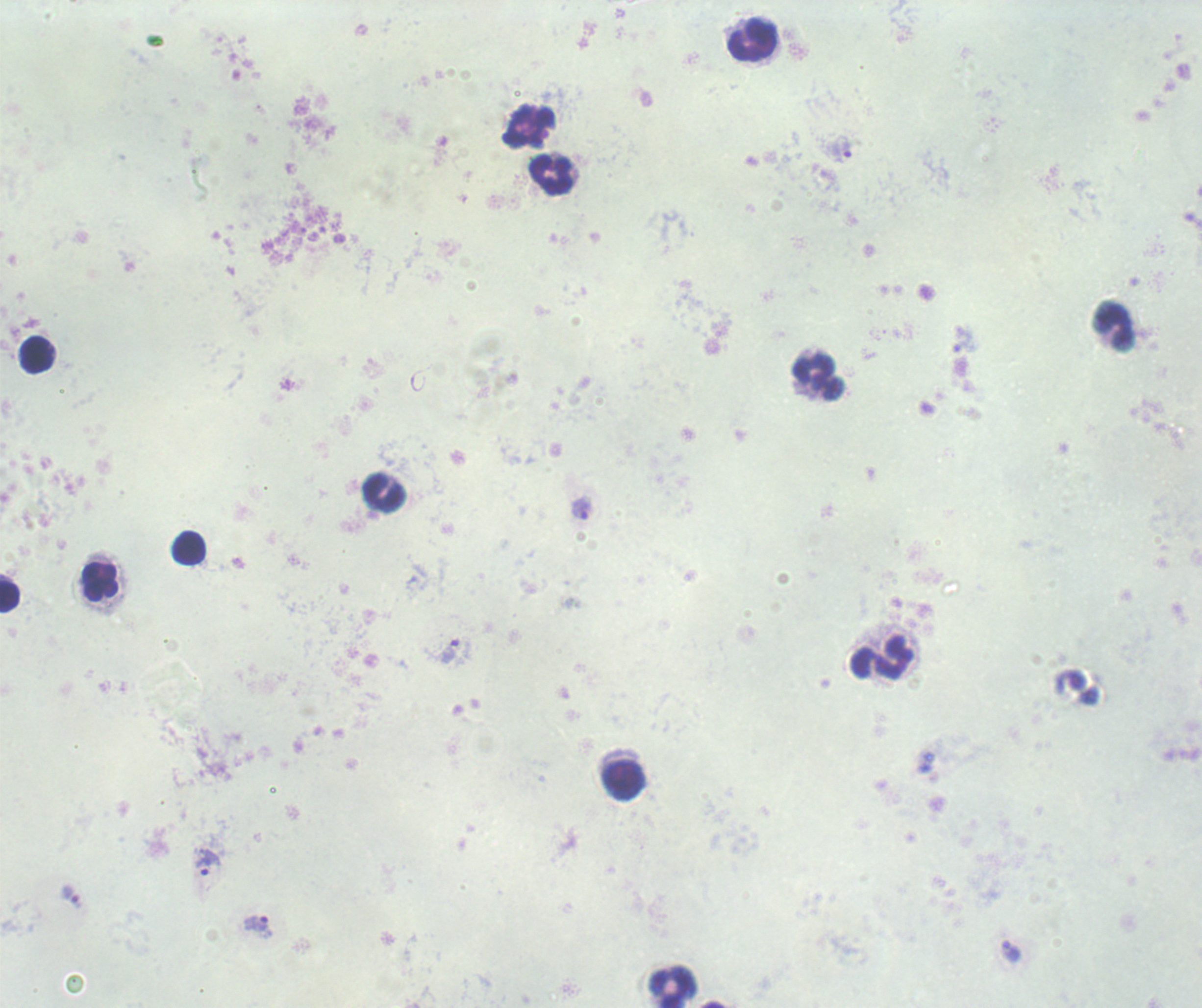
Approximate object centers, in pixels from the top-left corner. Trophozoite locations: (x=529, y=125), (x=841, y=149), (x=581, y=508), (x=449, y=651), (x=208, y=863), (x=71, y=896), (x=258, y=926), (x=1012, y=951). Leukocyte locations: (x=752, y=40), (x=550, y=174), (x=1113, y=327), (x=37, y=355), (x=818, y=376), (x=384, y=494), (x=189, y=547), (x=100, y=582), (x=10, y=597), (x=882, y=656), (x=623, y=781), (x=673, y=986). Single field of view. Previously used in an actual diagnosis. Captured at 100x magnification. Thick smear of blood. Image is 1202×1008 pixels. Romanowsky stain. Background quality: poor. Result: positive for Plasmodium parasites.